Point out each Plasmodium parasite.
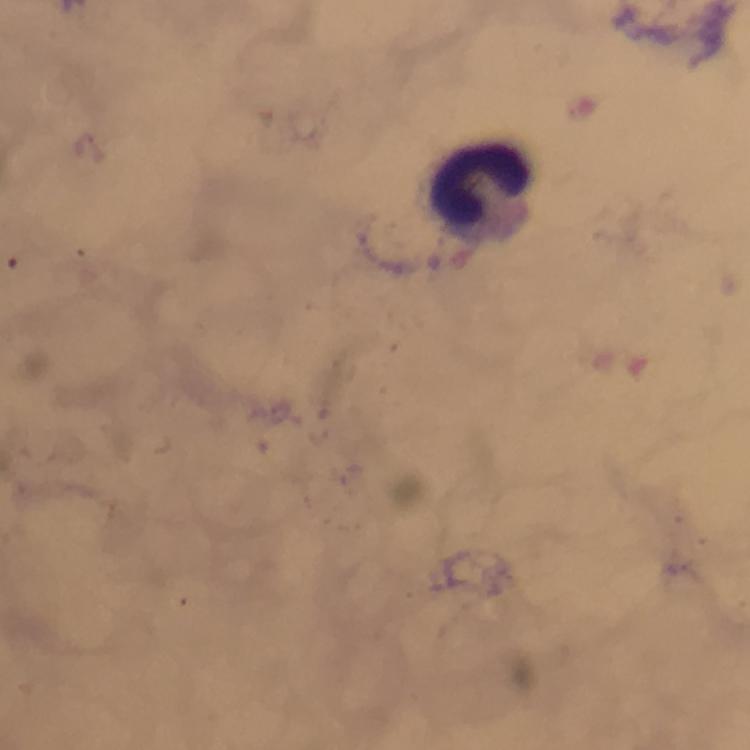
No Plasmodium parasites detected.

Approximate centers as {x, y} in pixels.
Summary:
  - Leukocyte locations: {483, 186}
  - Image size: 750×750 pixels
  - Capture: smartphone photograph through a microscope
  - Preparation: thick smear
  - Cropped from: one field of view
  - Context: from a malaria diagnostic workup
  - Immersion oil: used
  - Magnification: 100x
  - Stain: Giemsa